Identify the blood parasite species.
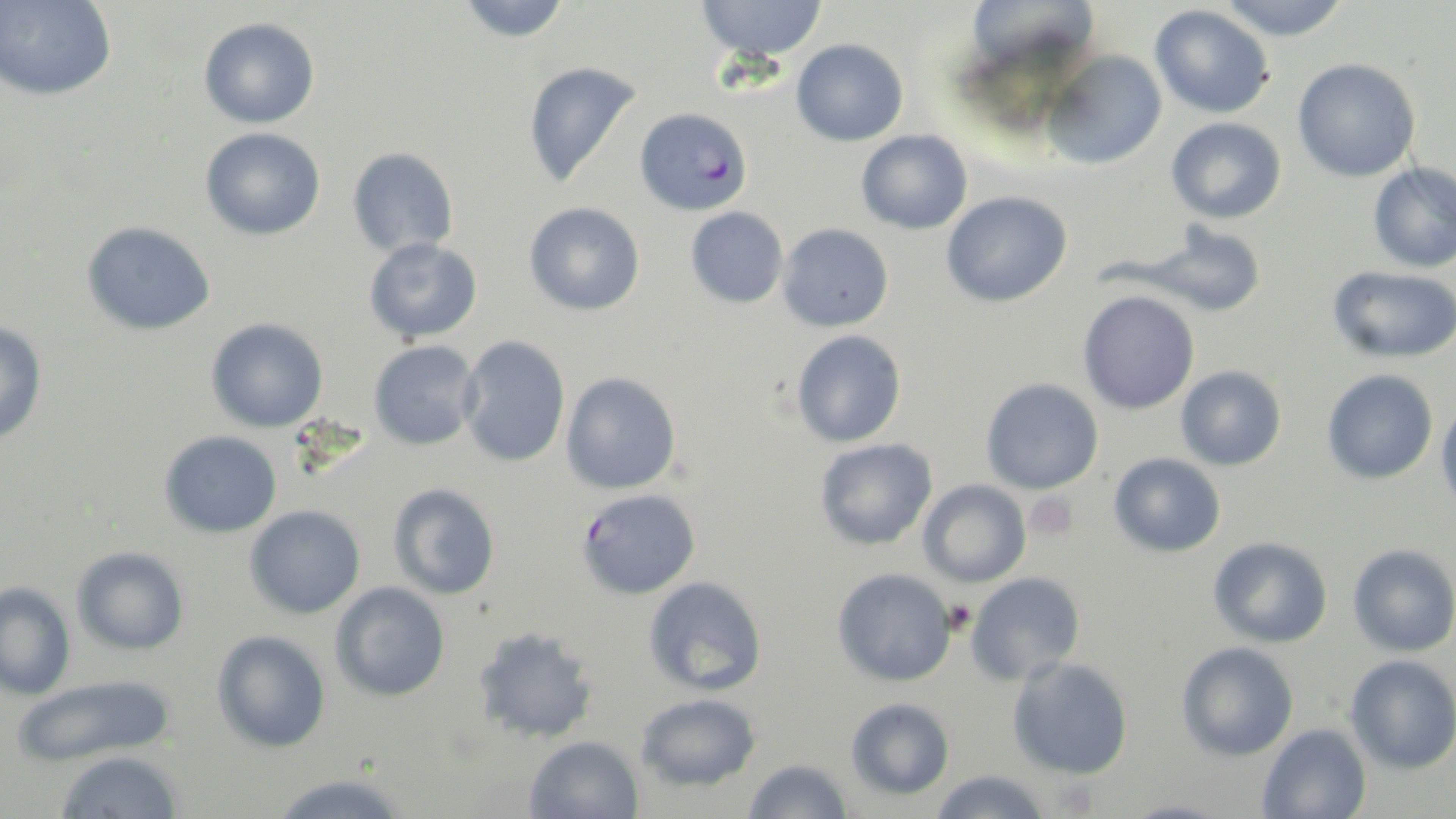
Plasmodium falciparum.

Summary:
  - Coordinate format: approximate bounding boxes as (x1,y1)-(x2,y2) corner pairs in pixels
  - Platelet locations: (1025,492)-(1080,542)
  - Uninfected red blood cell locations: (1,0)-(118,102), (456,0)-(571,43), (696,0)-(827,63), (1215,0)-(1351,40), (1149,4)-(1274,119), (198,17)-(321,129), (791,38)-(908,146), (1042,50)-(1167,169), (1292,57)-(1421,181), (521,60)-(645,188), (1166,117)-(1286,224), (200,127)-(326,240), (856,129)-(973,234), (347,147)-(459,258), (1367,162)-(1456,273), (941,191)-(1072,308), (524,202)-(645,316), (685,206)-(788,308), (80,220)-(216,336), (777,223)-(894,332), (1139,224)-(1267,317), (364,237)-(482,343), (1327,264)-(1456,364), (1077,290)-(1201,415), (0,318)-(48,447), (205,318)-(329,433), (791,329)-(907,448), (458,335)-(571,467), (368,339)-(481,451), (1175,365)-(1287,471), (1322,368)-(1439,485), (561,371)-(682,494), (981,377)-(1104,494), (1436,398)-(1456,523), (160,430)-(282,538), (814,438)-(939,551), (1109,452)-(1226,557), (918,479)-(1031,587), (387,482)-(501,600), (575,487)-(701,599), (244,505)-(366,619), (1208,536)-(1333,648), (1347,543)-(1456,657), (72,546)-(191,655), (831,567)-(957,687), (965,573)-(1086,685), (643,575)-(767,696), (0,581)-(76,701), (330,581)-(450,702), (472,625)-(600,744), (211,629)-(331,753), (1176,642)-(1300,762), (1344,654)-(1456,774), (1007,656)-(1134,780), (10,673)-(178,768), (636,692)-(762,792), (846,697)-(955,800), (1257,723)-(1372,819), (523,735)-(645,819), (55,750)-(183,818), (742,758)-(854,819), (928,769)-(1053,819), (268,771)-(415,817), (1120,797)-(1237,819)
  - Plasmodium falciparum-infected red blood cell locations: (634,107)-(753,216)
  - Stain: May-Grünwald-Giemsa
  - Preparation: thin blood film
  - Image size: 1456×819 pixels
  - Magnification: 1000x
  - Modality: light microscopy
  - Field of view: single